Report the malaria status of this cell.
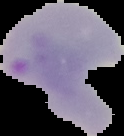

It is parasitized.

preparation = thin blood smear
image size = 124×136 pixels
image type = cell region segmented out of the field of view; surrounding area masked to black